Assess the morphology of the erythrocytes.
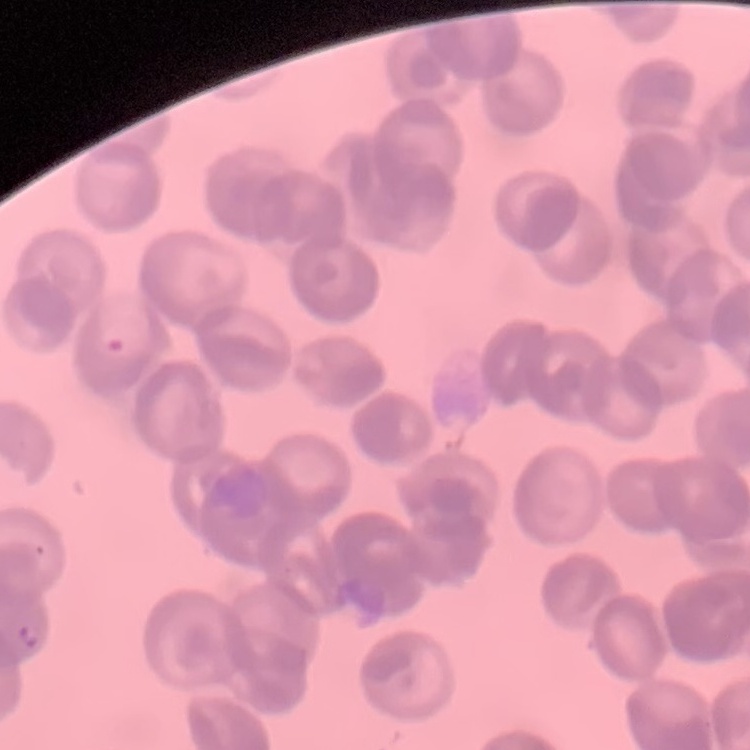

Rouleaux formation.

One tile cut from a larger photomicrograph. Thin peripheral smear. Stained with either Field's or Giemsa.